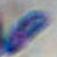
Summary:
  - Identification: Toxoplasma gondii
  - Magnification: 1000x
  - Modality: micrograph